Comment on the morphology of the erythrocytes.
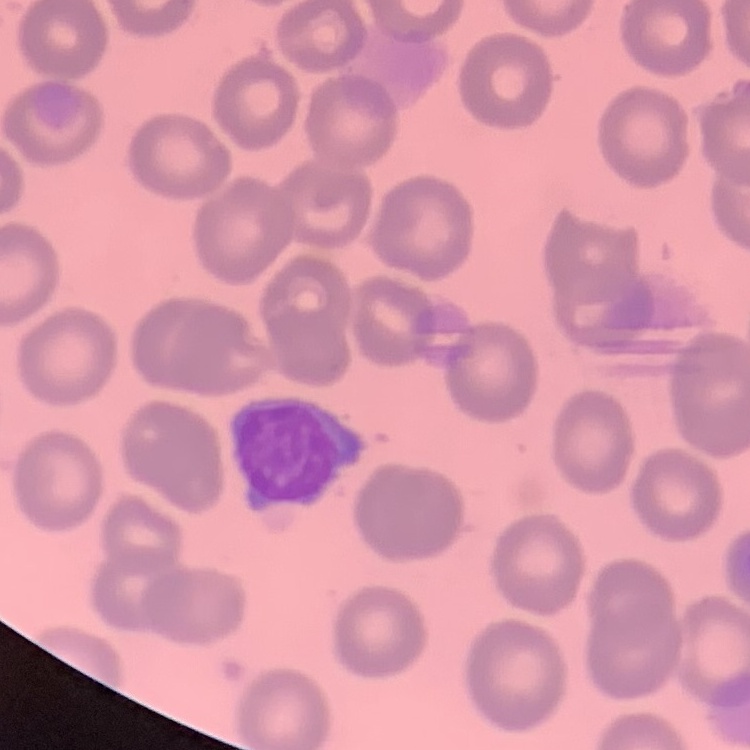
No rouleaux formation.

Field's or Giemsa stain. Thin blood film. Square crop of a larger photomicrograph.